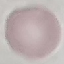
{
  "result": "negative for malaria parasites",
  "stain": "Giemsa",
  "capture": "smartphone camera at the microscope eyepiece",
  "preparation": "thin blood smear",
  "image_type": "cell patch, automatically extracted from a larger field of view and resized to 64 × 64 pixels"
}